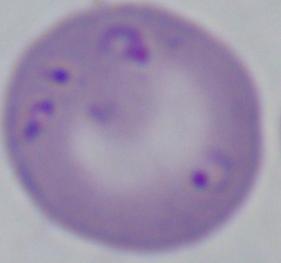
modality = micrograph
magnification = 1000x
identification = Babesia